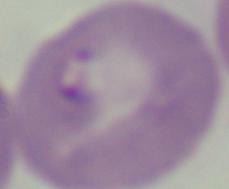
magnification: 1000x
identification: Babesia
modality: photomicrograph